Assess this cell for malaria.
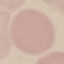

Uninfected.

Summary:
  - Capture: smartphone through the microscope eyepiece
  - Image type: cell patch, automatically extracted from a larger field of view and resized to 64 × 64 pixels
  - Preparation: thin blood smear
  - Stain: Giemsa